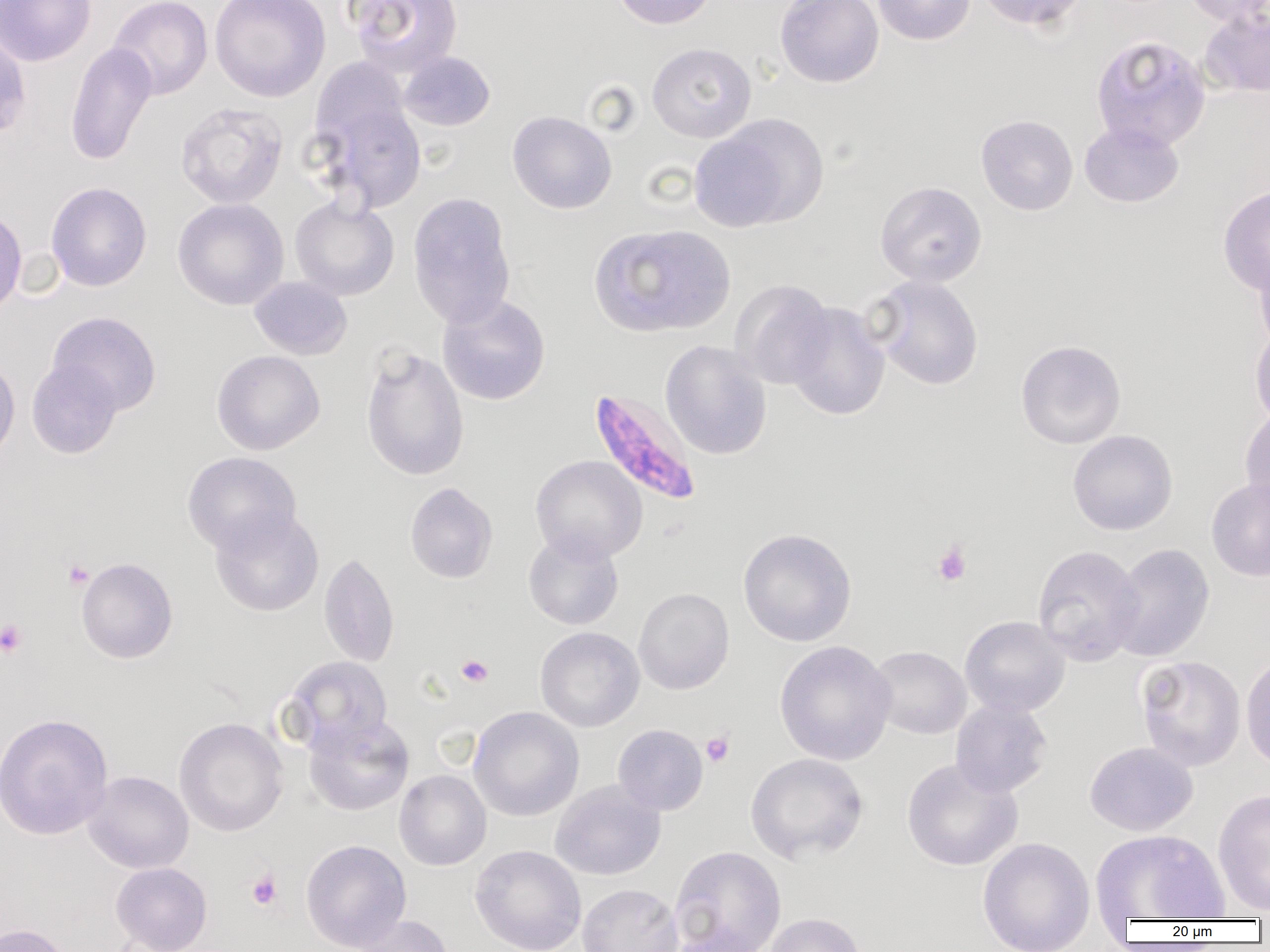

{
  "slide_level_diagnosis": "Plasmodium falciparum",
  "modality": "optical microscopy",
  "field_of_view": "one of a larger specimen",
  "preparation": "thin blood film",
  "image_size": "1270×952 pixels",
  "platelet_locations": "approximate bounding boxes as (x1, y1, x2, y2) in pixels: (931, 541, 972, 586), (64, 560, 93, 590), (0, 619, 28, 657), (456, 654, 493, 687), (701, 731, 734, 767), (246, 869, 283, 912)",
  "magnification": "1000x",
  "uninfected_red_blood_cell_locations": "approximate bounding boxes as (x1, y1, x2, y2) in pixels: (0, 0, 97, 66), (108, 0, 213, 100), (209, 0, 330, 102), (345, 0, 463, 78), (611, 0, 716, 29), (775, 0, 884, 88), (873, 0, 975, 45), (976, 0, 1088, 31), (1183, 0, 1270, 27), (1199, 6, 1270, 98), (0, 34, 31, 139), (1091, 35, 1211, 151), (65, 41, 157, 166), (646, 42, 756, 143), (399, 51, 496, 131), (310, 83, 427, 214), (175, 102, 288, 209), (507, 110, 617, 214), (976, 114, 1078, 216), (693, 115, 828, 231), (1079, 121, 1184, 207), (875, 181, 987, 287), (46, 182, 152, 292), (1218, 185, 1270, 296), (407, 192, 517, 328), (289, 197, 400, 300), (172, 198, 289, 310), (0, 207, 27, 317), (589, 223, 736, 338), (1254, 251, 1270, 355), (870, 275, 984, 390), (249, 276, 352, 360), (730, 279, 836, 390), (437, 294, 551, 406), (786, 302, 890, 421), (47, 311, 162, 417), (1249, 327, 1270, 428), (1015, 339, 1126, 449), (660, 340, 772, 460), (360, 346, 470, 481), (211, 349, 326, 455), (0, 357, 20, 467), (26, 359, 123, 459), (1240, 405, 1270, 515), (1067, 430, 1178, 536), (182, 451, 302, 555), (530, 455, 648, 563), (1206, 477, 1270, 581), (405, 482, 498, 583), (209, 507, 325, 617), (737, 528, 857, 647), (523, 530, 624, 630), (1108, 543, 1215, 663), (1032, 544, 1144, 666), (319, 552, 400, 667), (75, 557, 178, 663), (633, 587, 734, 695), (960, 615, 1071, 717), (535, 626, 645, 732), (774, 640, 897, 766), (867, 645, 971, 739), (1241, 652, 1270, 771), (1135, 655, 1247, 772), (285, 656, 393, 751), (951, 699, 1053, 798), (468, 706, 584, 821), (0, 712, 113, 840), (303, 713, 414, 816), (174, 717, 288, 837), (613, 724, 708, 815), (1084, 741, 1198, 836), (745, 752, 869, 864), (901, 758, 1023, 871), (394, 769, 491, 870), (83, 770, 194, 874), (550, 780, 666, 881), (1212, 788, 1270, 914), (1090, 829, 1228, 921), (977, 837, 1095, 952), (301, 839, 411, 951), (470, 844, 586, 952), (669, 845, 787, 952), (111, 862, 212, 952), (577, 883, 683, 952), (763, 912, 867, 952), (348, 915, 456, 952), (0, 923, 74, 952), (663, 926, 774, 952)",
  "plasmodium_falciparum_infected_red_blood_cell_locations": "approximate bounding boxes as (x1, y1, x2, y2) in pixels: (588, 388, 702, 507)"
}